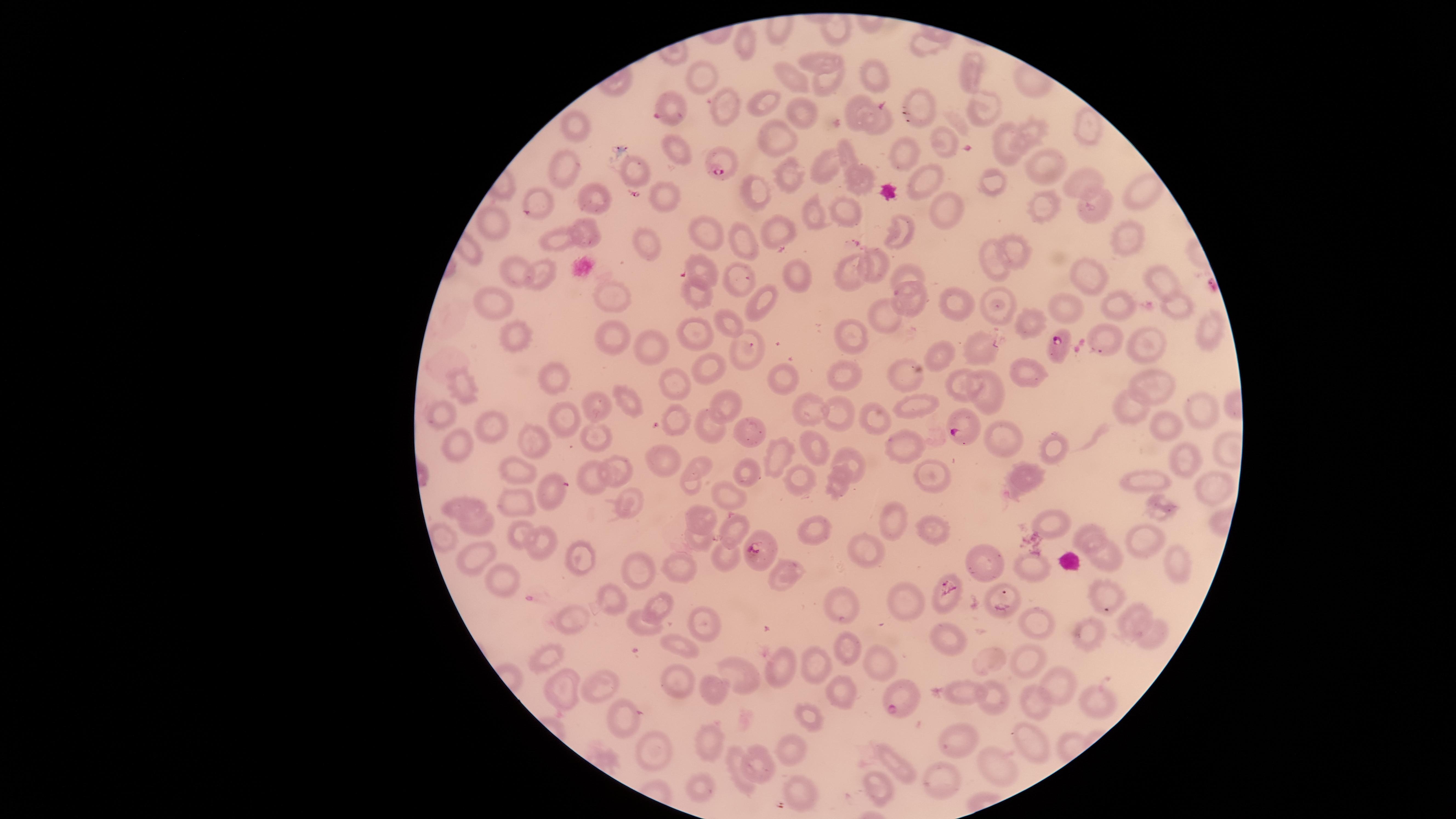
Approximate marker points as [x, y] in pixels. Uninfected red blood cells: [834, 31], [748, 42], [923, 45], [818, 59], [971, 71], [873, 72], [796, 77], [707, 78], [824, 82], [925, 94], [767, 101], [857, 103], [976, 104], [723, 107], [803, 114], [883, 121], [1035, 127], [571, 129], [1082, 129], [770, 139], [945, 139], [1003, 144], [679, 151], [849, 152], [906, 154], [822, 164], [1053, 165], [631, 169], [563, 174], [996, 178], [788, 179], [925, 182], [1079, 182], [862, 183], [1134, 193], [755, 195], [537, 198], [666, 199], [593, 201], [1096, 202], [849, 208], [1043, 208], [952, 210], [813, 213], [499, 223], [703, 229], [779, 230], [898, 230], [1127, 232], [592, 234], [744, 241], [560, 242], [640, 242], [1014, 245], [877, 260], [991, 266], [700, 268], [804, 272], [908, 274], [546, 275], [519, 276], [853, 278], [1091, 279], [1159, 279], [738, 280], [612, 290], [699, 294], [913, 294], [756, 300], [502, 304], [1175, 304], [1118, 305], [951, 306], [1067, 309], [885, 315], [996, 317], [729, 320], [1026, 322], [1207, 336], [512, 338], [698, 338], [850, 338], [604, 340], [654, 341], [1103, 342], [1141, 343], [981, 347], [749, 349], [942, 355], [713, 368], [1017, 369], [854, 375], [558, 379], [786, 380], [1152, 380], [679, 383], [903, 384], [463, 388], [996, 390], [963, 392], [629, 399], [725, 400], [1129, 406], [915, 407], [600, 408], [811, 411], [1205, 411], [438, 414], [841, 416], [875, 420], [564, 422], [677, 423], [712, 425], [1160, 425], [491, 427], [751, 430], [592, 439], [999, 441], [460, 444], [902, 444], [533, 445], [1050, 446], [776, 453], [821, 453], [665, 463], [1189, 464], [848, 465], [702, 467], [623, 471], [516, 472], [747, 475], [586, 476], [793, 479], [936, 479], [1019, 480], [1147, 480], [547, 484], [691, 485], [835, 485], [1207, 485], [727, 498], [513, 500], [625, 500], [450, 507], [1162, 507], [700, 520], [895, 522], [1050, 522], [482, 525], [926, 527], [730, 529], [815, 531], [523, 535], [444, 536], [699, 543], [1140, 544], [540, 545], [866, 550], [474, 556], [581, 556], [726, 560], [1180, 560], [984, 564], [640, 567], [679, 567], [1028, 568], [785, 575], [496, 577], [1108, 594], [944, 600], [845, 601], [611, 602], [999, 602], [659, 605], [916, 606], [1132, 620], [640, 621], [1035, 621], [574, 624], [698, 624], [1090, 630], [945, 633], [1153, 635], [683, 645], [852, 650], [989, 656], [546, 660], [879, 661], [780, 664], [1026, 664], [817, 665], [741, 674], [676, 683], [1059, 686], [594, 687], [558, 688], [840, 689], [965, 695], [998, 698], [1029, 705], [1096, 707], [621, 715], [808, 716], [1028, 739], [709, 740], [962, 745], [655, 753], [791, 753], [759, 760], [892, 763], [740, 768], [992, 770], [941, 781], [877, 785], [696, 786], [798, 789]. Parasitized red blood cells: [664, 111], [718, 160], [1059, 348], [956, 430], [760, 549], [905, 701]. Presence: malaria parasites identified. Thin smear of blood. One field of view of the specimen. Image is 1456×819 pixels. Species: Plasmodium falciparum. Giemsa-stained preparation. Smartphone photograph through the microscope eyepiece. The visible region is circular.